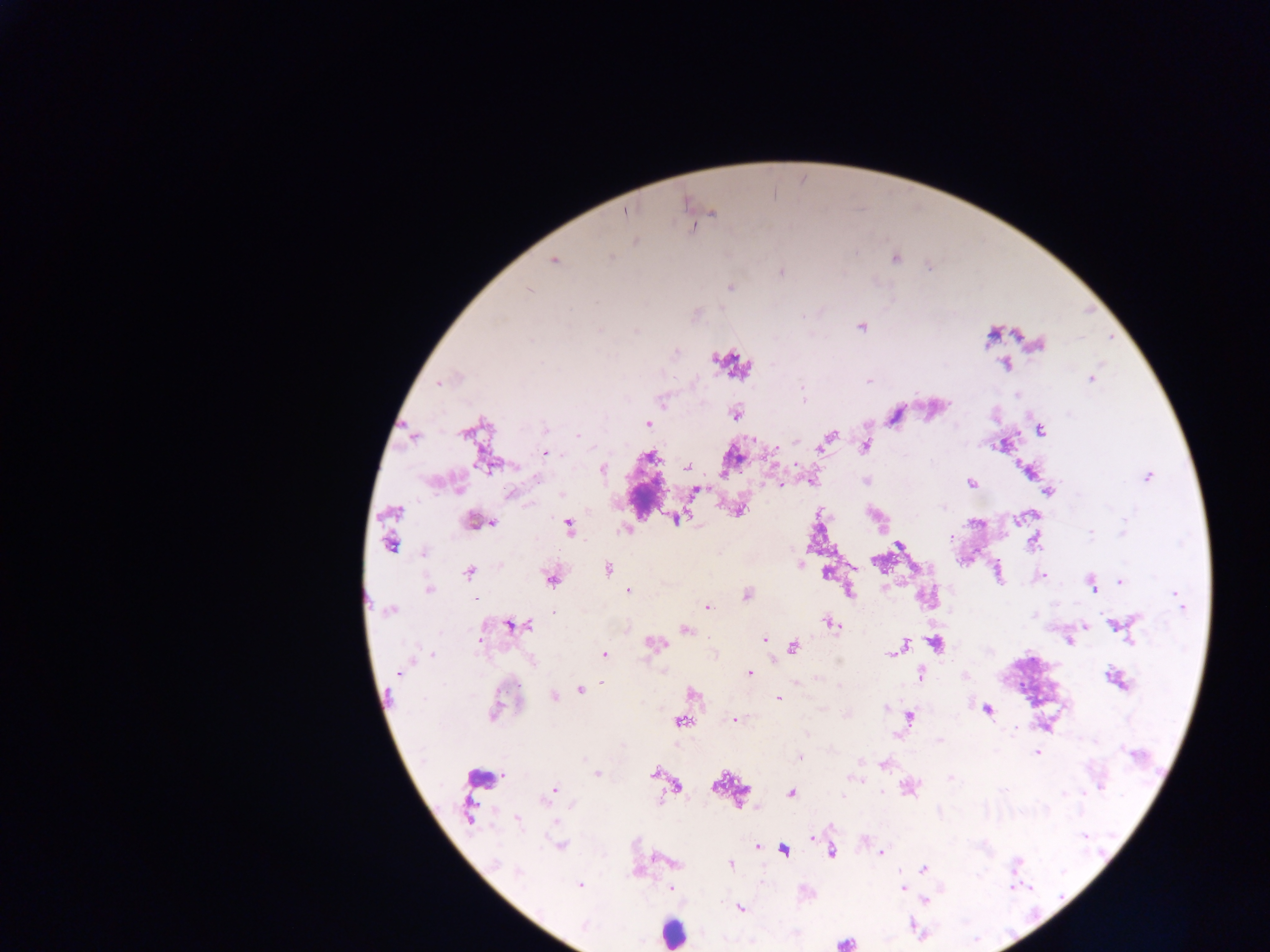
Approximate centers as x y in pixels.
Summary:
  - Plasmodium parasite locations: 626 213; 713 213; 635 241; 611 256; 894 258; 554 261; 781 272; 730 287; 528 291; 861 326; 599 330; 1038 344; 1004 365; 1092 378; 439 382; 869 382; 803 398; 662 401; 735 415; 648 424; 546 429; 1041 430; 578 435; 413 436; 829 438; 1003 445; 864 447; 546 452; 649 457; 488 465; 687 467; 603 470; 1147 477; 537 478; 812 481; 971 484; 458 487; 697 490; 1049 491; 560 494; 511 495; 739 511; 394 512; 676 518; 474 523; 493 524; 569 526; 625 530; 1123 531; 1091 533; 950 538; 1034 541; 389 546; 898 546; 424 553; 800 563; 607 568; 998 572; 469 573; 827 573; 1043 575; 550 579; 1121 580; 1092 584; 429 590; 628 592; 849 592; 746 595; 1179 599; 707 607; 391 610; 554 612; 831 624; 515 626; 1084 626; 1117 626; 685 629; 764 639; 1131 639; 1069 641; 655 643; 936 643; 903 646; 793 647; 897 650; 892 653; 605 654; 432 655; 399 672; 749 674; 921 675; 1117 680; 602 684; 580 690; 693 694; 554 696; 779 699; 885 708; 987 710; 493 713; 910 718; 734 719; 681 722; 939 740; 1036 753; 1133 754; 799 757; 584 760; 860 761; 885 764; 654 773; 597 774; 950 778; 856 779; 717 785; 1101 785; 678 787; 910 788; 551 793; 791 793; 1065 794; 468 811; 518 822; 560 845; 756 846; 783 850; 832 852; 881 853; 668 861; 496 863; 731 864; 1016 865; 924 868; 519 872; 580 886; 671 888; 903 888; 926 900; 741 908; 584 926; 844 943
  - Leukocyte locations: 647 499; 479 781; 673 932
  - Capture: mobile-phone photograph through a microscope
  - Field of view: single
  - Image size: 1270×952 pixels
  - Country: Ghana
  - Preparation: thick blood smear